Identify the preparation type.
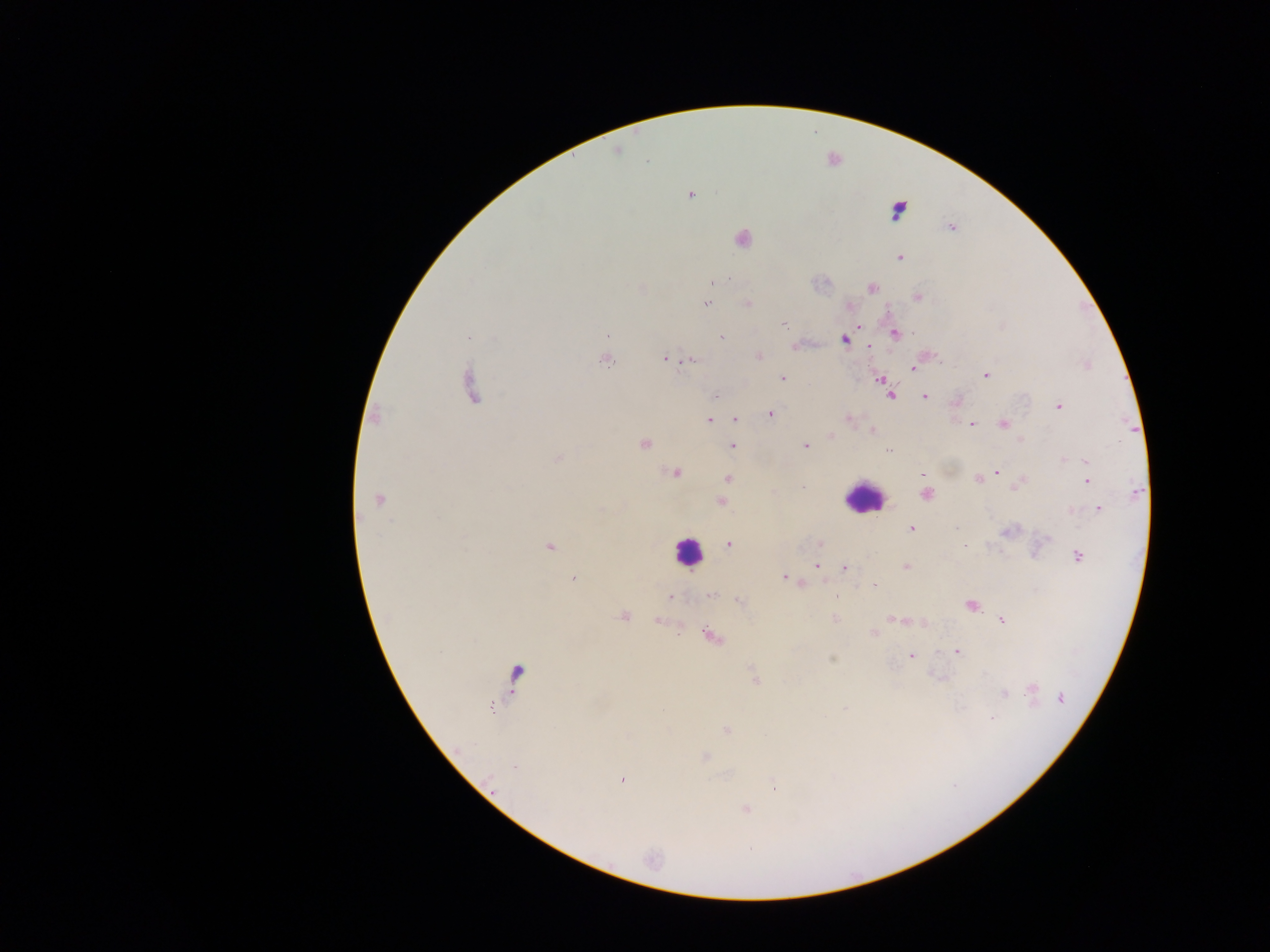
This is a thick smear.

Approximate centers as [x, y] in pixels.
Summary:
  - Plasmodium parasite locations: [617, 151], [647, 162], [690, 194], [950, 227], [741, 238], [899, 257], [872, 288], [916, 296], [706, 304], [746, 304], [847, 306], [783, 324], [860, 326], [894, 333], [608, 335], [469, 336], [721, 338], [844, 339], [796, 346], [868, 346], [758, 356], [604, 359], [663, 359], [690, 359], [914, 368], [986, 375], [782, 378], [878, 379], [470, 388], [886, 388], [717, 395], [890, 395], [925, 396], [957, 401], [1058, 406], [770, 413], [375, 416], [733, 418], [847, 418], [708, 420], [971, 424], [1003, 424], [870, 431], [830, 436], [644, 443], [805, 445], [733, 446], [888, 450], [557, 457], [1086, 462], [997, 471], [674, 474], [922, 474], [726, 478], [978, 480], [1087, 481], [1018, 484], [803, 486], [1136, 493], [925, 494], [378, 499], [720, 502], [1099, 509], [911, 528], [1008, 531], [819, 542], [728, 544], [549, 545], [1076, 556], [816, 565], [905, 567], [845, 568], [783, 576], [573, 578], [800, 582], [710, 596], [670, 598], [740, 601], [971, 606], [623, 615], [834, 618], [895, 619], [1001, 619], [657, 622], [924, 624], [874, 632], [708, 634], [956, 651], [910, 655], [516, 673], [755, 679], [1032, 690], [1003, 693], [1060, 698], [846, 708], [726, 730], [704, 756], [622, 780], [773, 787], [746, 810]
  - Leukocyte locations: [897, 209], [864, 497], [687, 552]
  - Capture: mobile-phone photograph through a microscope
  - Country: Ghana
  - Field of view: single
  - Image size: 1270×952 pixels